Classify this cell by malaria status.
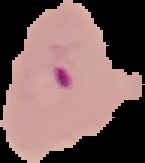
It is parasitized.

Segmented cell region on a black background. From a thin blood smear. Image is 145×163 pixels.